Describe the morphology of the erythrocytes.
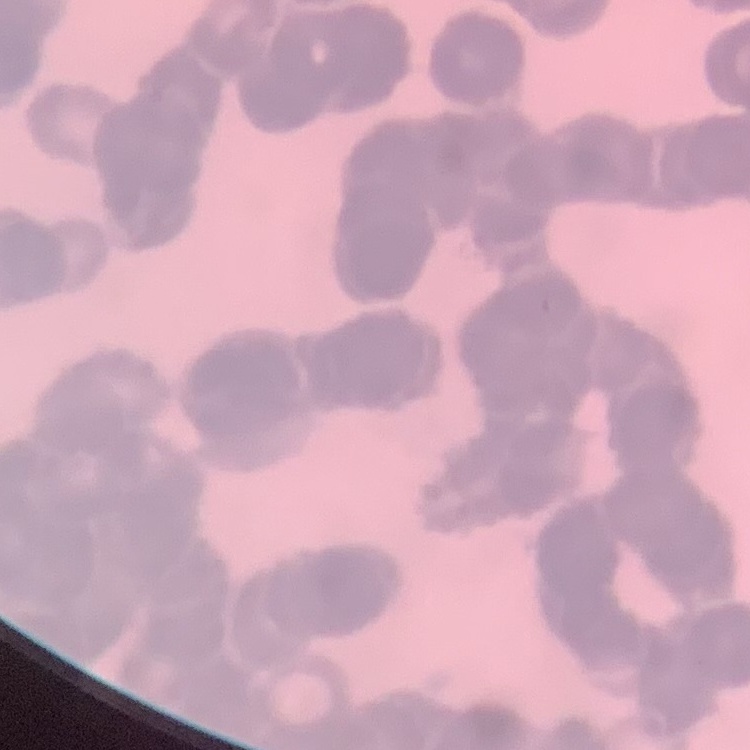

They show rouleaux formation.

Stained with either Field's or Giemsa. One tile cut from a larger photomicrograph. Thin peripheral smear.